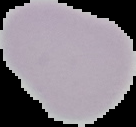
From a thin blood film. Image is 136×127 pixels. Malaria status: uninfected. Cell region segmented out of the field of view; the surrounding area is masked to black.